Identify the parasite.
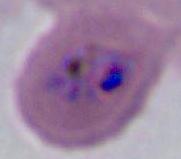
Plasmodium.

magnification = 400x or 1000x
modality = photomicrograph